Outline each Plasmodium falciparum-infected red blood cell.
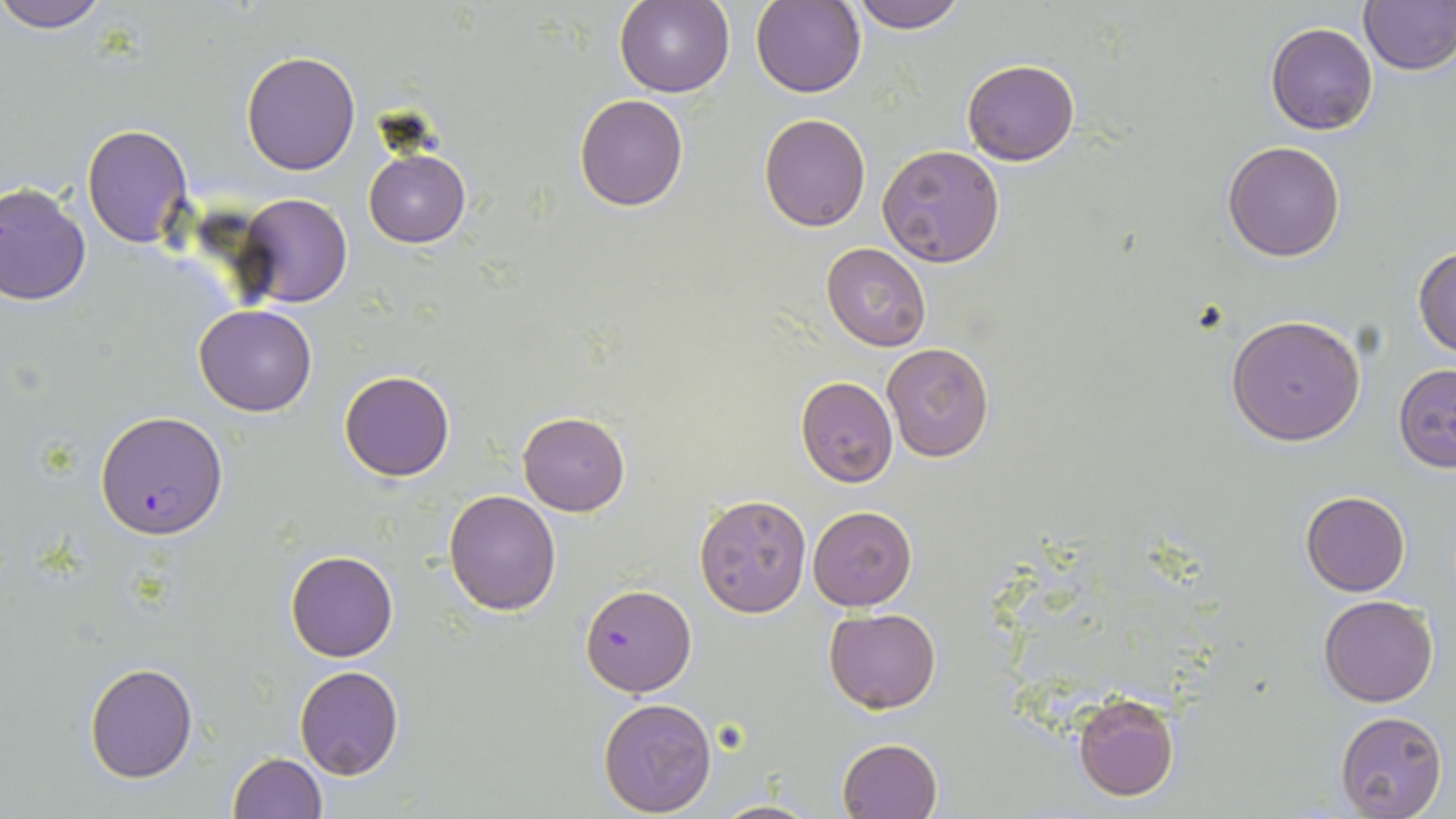

Approximate bounding boxes as (x1, y1, x2, y2) in pixels.
Plasmodium falciparum-infected red blood cells: (95, 410, 227, 538), (581, 583, 696, 697).

slide-level diagnosis = Plasmodium falciparum
image size = 1456×819 pixels
field of view = single
magnification = 1000x
preparation = thin blood smear
uninfected red blood cell locations = approximate bounding boxes as (x1, y1, x2, y2) in pixels: (1, 0, 111, 32), (851, 0, 966, 33), (1357, 0, 1456, 74), (614, 1, 736, 98), (752, 1, 866, 98), (1265, 21, 1378, 135), (241, 51, 360, 174), (962, 60, 1079, 165), (573, 94, 689, 211), (757, 112, 871, 232), (81, 123, 193, 249), (1222, 140, 1347, 261), (877, 143, 1005, 266), (364, 149, 470, 248), (0, 181, 92, 304), (237, 193, 353, 309), (822, 242, 931, 351), (1413, 244, 1456, 362), (195, 304, 316, 416), (1225, 313, 1368, 446), (881, 342, 994, 462), (1391, 364, 1456, 471), (339, 370, 455, 481), (795, 377, 898, 488), (517, 410, 631, 517), (444, 489, 562, 614), (1300, 490, 1410, 595), (694, 492, 813, 618), (809, 505, 917, 612), (285, 551, 399, 661), (1319, 595, 1439, 706), (824, 609, 941, 713), (84, 662, 198, 783), (294, 665, 404, 781), (1071, 693, 1179, 802), (598, 697, 716, 816), (1336, 710, 1447, 819), (837, 736, 943, 819), (227, 752, 327, 819), (711, 798, 820, 819)
stain = May-Grünwald-Giemsa
modality = optical microscopy